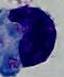

magnification = 1000x
identification = white blood cell
modality = photomicrograph